Assess for Plasmodium parasites.
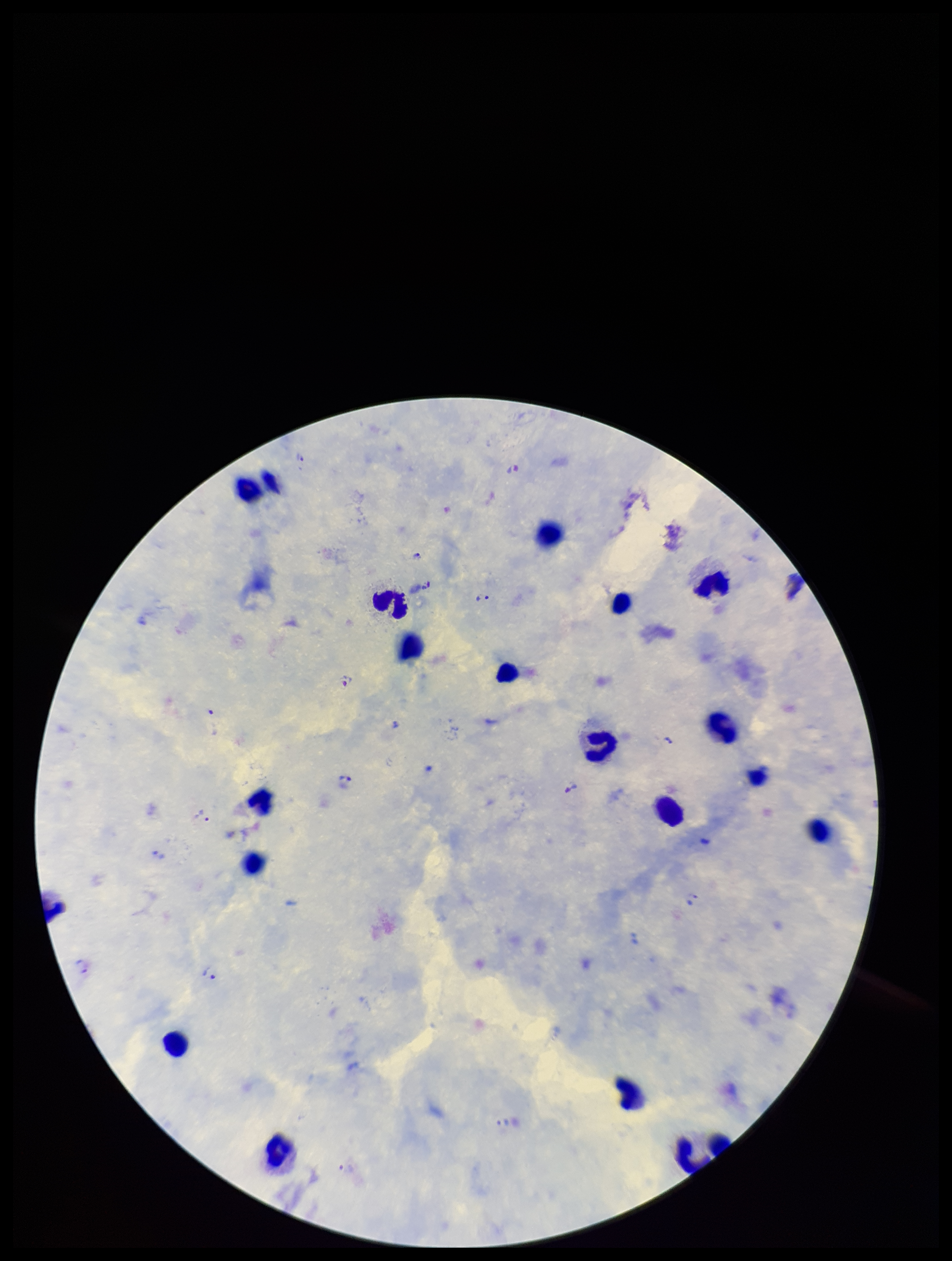
Detected.

Summary:
  - Field of view: single
  - Capture: smartphone photograph through the microscope eyepiece
  - Patient malaria status: infected
  - Image size: 952×1261 pixels
  - Preparation: thick
  - Parasite count: 18
  - Stain: Giemsa
  - Species reported for this patient: Plasmodium vivax
  - Leukocyte count: 20